Locate every blood parasite and identify its species.
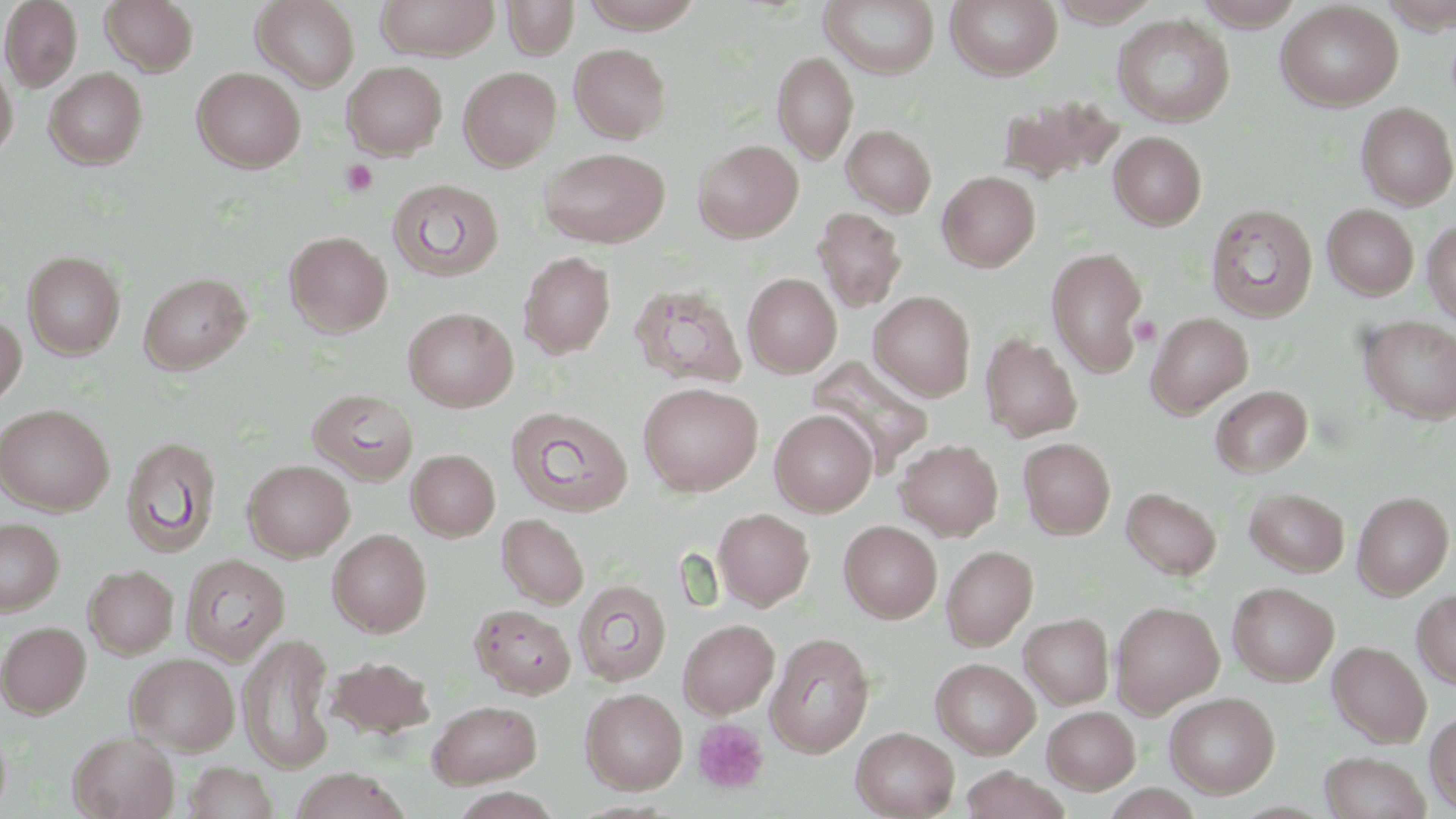

No blood parasites observed.

Summary:
  - Coordinate format: approximate bounding boxes as (x1, y1, x2, y2) in pixels
  - Platelet locations: (341, 159, 378, 197), (1130, 316, 1161, 346), (693, 718, 770, 795)
  - Uninfected red blood cell locations: (0, 0, 83, 91), (101, 0, 199, 75), (252, 0, 360, 92), (376, 0, 500, 60), (503, 0, 580, 59), (580, 0, 704, 32), (945, 0, 1062, 80), (1194, 0, 1303, 29), (1378, 0, 1456, 32), (820, 1, 940, 78), (1047, 1, 1161, 27), (1276, 2, 1402, 111), (1113, 14, 1235, 127), (570, 43, 671, 142), (773, 51, 858, 163), (342, 61, 447, 159), (0, 62, 18, 162), (192, 67, 305, 172), (459, 67, 561, 170), (44, 68, 147, 169), (997, 93, 1125, 186), (1356, 102, 1456, 210), (841, 124, 937, 217), (1108, 131, 1207, 230), (694, 139, 803, 242), (538, 147, 669, 248), (938, 170, 1040, 271), (387, 179, 504, 281), (1205, 204, 1317, 322), (1322, 204, 1419, 299), (813, 206, 907, 312), (1422, 221, 1456, 324), (284, 231, 393, 337), (1045, 246, 1149, 377), (23, 251, 126, 359), (518, 251, 616, 359), (138, 272, 251, 375), (743, 273, 841, 377), (630, 283, 747, 389), (869, 291, 976, 401), (403, 307, 518, 411), (1146, 312, 1253, 417), (0, 314, 26, 410), (1358, 316, 1456, 425), (980, 334, 1082, 442), (807, 357, 935, 473), (638, 382, 763, 496), (1210, 385, 1313, 477), (308, 388, 419, 484), (0, 403, 114, 516), (506, 406, 632, 517), (770, 410, 876, 516), (120, 436, 222, 559), (1018, 437, 1115, 539), (896, 439, 1003, 540), (406, 449, 500, 541), (242, 459, 355, 561), (1121, 487, 1221, 579), (1244, 487, 1350, 576), (1352, 491, 1454, 599), (713, 508, 814, 609), (497, 513, 589, 609), (0, 517, 64, 615), (839, 520, 942, 623), (327, 529, 432, 637), (941, 545, 1038, 650), (180, 554, 290, 662), (84, 564, 178, 659), (573, 579, 672, 686), (1228, 582, 1338, 686), (1412, 589, 1456, 688), (1110, 600, 1224, 716), (470, 603, 577, 698), (1019, 613, 1114, 709), (678, 618, 780, 718), (0, 621, 91, 717), (765, 632, 875, 757), (238, 633, 337, 774), (1328, 640, 1431, 747), (126, 653, 240, 755), (327, 655, 435, 740), (931, 657, 1040, 759), (580, 687, 688, 794), (1164, 692, 1280, 798), (428, 699, 542, 788), (1042, 706, 1140, 794), (1425, 711, 1456, 812), (0, 723, 12, 817), (851, 726, 959, 819), (68, 731, 180, 819), (1320, 750, 1431, 819), (183, 761, 279, 819), (959, 766, 1070, 819), (290, 768, 411, 819), (1100, 783, 1208, 818)
  - Slide-level diagnosis: no evidence of blood parasites
  - Stain: May-Grünwald-Giemsa
  - Image size: 1456×819 pixels
  - Magnification: 1000x
  - Field of view: single
  - Modality: optical microscopy
  - Preparation: thin blood film